Classify this cell by malaria status.
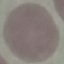

Uninfected.

Photographed with a smartphone camera at the microscope eyepiece. Automatically extracted cell patch, resized to 64 × 64 pixels. Thin smear of blood. Giemsa stain.